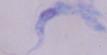
Captured at 1000x magnification. A trypanosome is shown. Photomicrograph.